Point out each leukocyte.
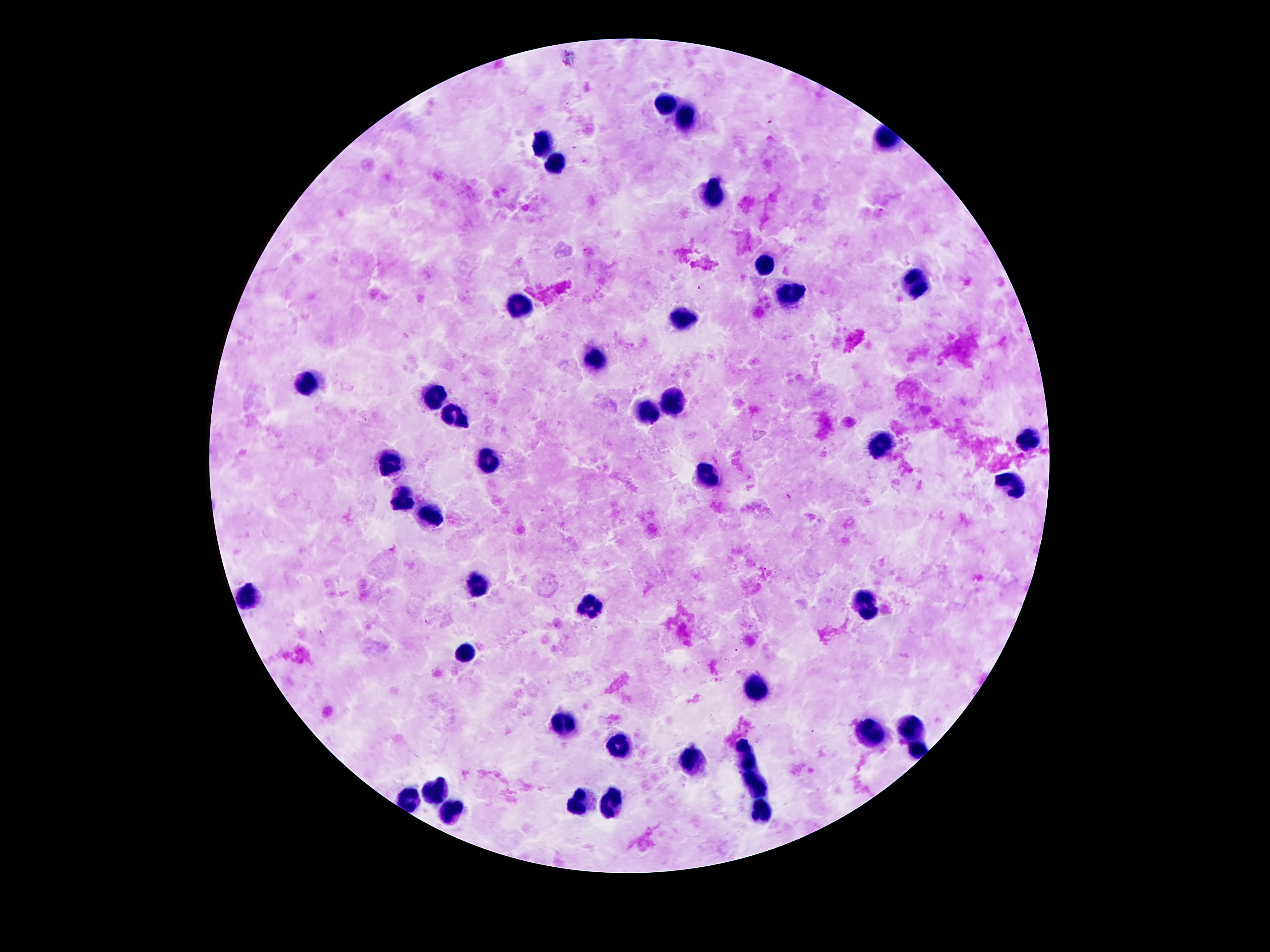

Approximate object centers, in pixels from the top-left corner.
Leukocytes: (x=665, y=106), (x=686, y=117), (x=544, y=141), (x=552, y=159), (x=707, y=196), (x=767, y=264), (x=916, y=285), (x=790, y=294), (x=526, y=311), (x=685, y=317), (x=597, y=357), (x=310, y=385), (x=436, y=396), (x=673, y=401), (x=646, y=412), (x=455, y=419), (x=1029, y=443), (x=882, y=446), (x=494, y=459), (x=392, y=461), (x=710, y=477), (x=1008, y=483), (x=405, y=500), (x=431, y=512), (x=478, y=584), (x=250, y=593), (x=869, y=605), (x=591, y=608), (x=466, y=655), (x=756, y=685), (x=566, y=724), (x=914, y=724), (x=867, y=732), (x=620, y=747), (x=916, y=752), (x=748, y=755), (x=690, y=761), (x=754, y=785), (x=438, y=790), (x=407, y=800), (x=611, y=800), (x=582, y=801), (x=453, y=806), (x=762, y=812).

{
  "image_size": "1270×952 pixels",
  "magnification": "100x",
  "patient_malaria_status": "negative",
  "stain": "Giemsa",
  "field_of_view": "single",
  "preparation": "thick peripheral-blood smear",
  "capture": "smartphone camera through the microscope eyepiece"
}